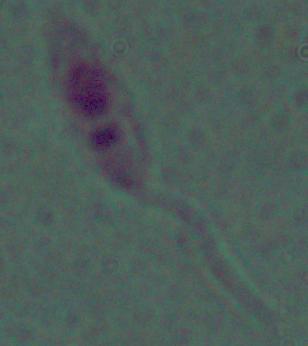

Summary:
  - Magnification: 1000x
  - Modality: micrograph
  - Identification: Leishmania